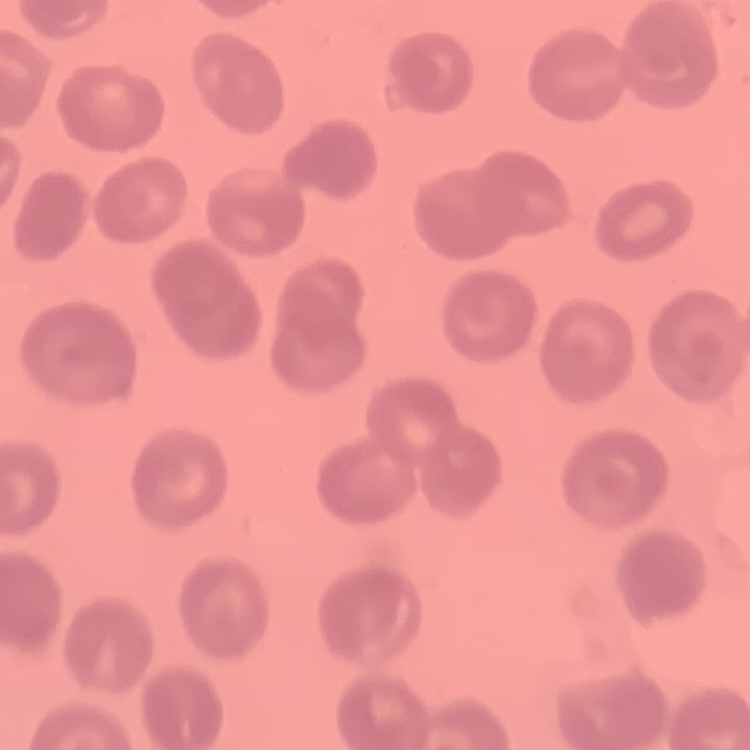

The red blood cells exhibit no rouleaux formation. Thin blood film. One tile cut from a larger photomicrograph. Stained with either Field's or Giemsa.